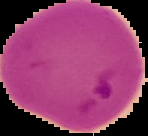

Summary:
  - Preparation: thin blood smear
  - Malaria status: parasitized
  - Image type: segmented cell region on a black background
  - Image size: 148×136 pixels